Give the position of every Plasmodium falciparum parasite, noting its life-cycle stage.
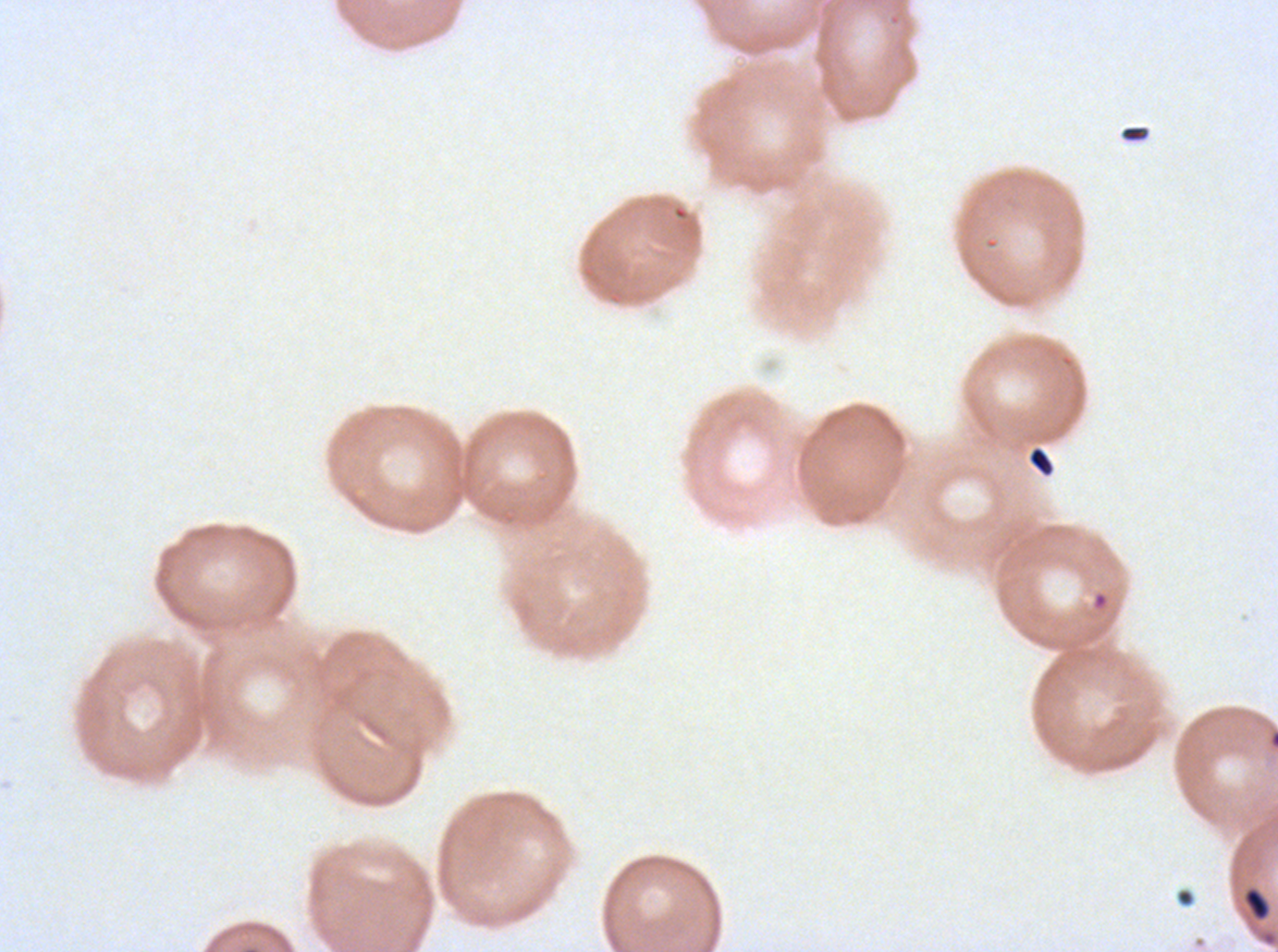
No rings, late-ring/early-trophozoite forms, mid trophozoites, late trophozoites, early schizonts, late schizonts, segmenters, or gametocytes observed.

Approximate bounding boxes as (x1, y1, x2, y2) in pixels. Debris locations: (1120, 125, 1149, 143), (1028, 446, 1053, 475), (1244, 887, 1270, 921). Giemsa-stained preparation. Thin blood film. Plasmodium falciparum cultured ex vivo for 24 to 48 hours, from a patient in The Gambia. A sub-image separated from a larger composite. Image is 1278×952 pixels.